Assess the morphology of the red blood cells.
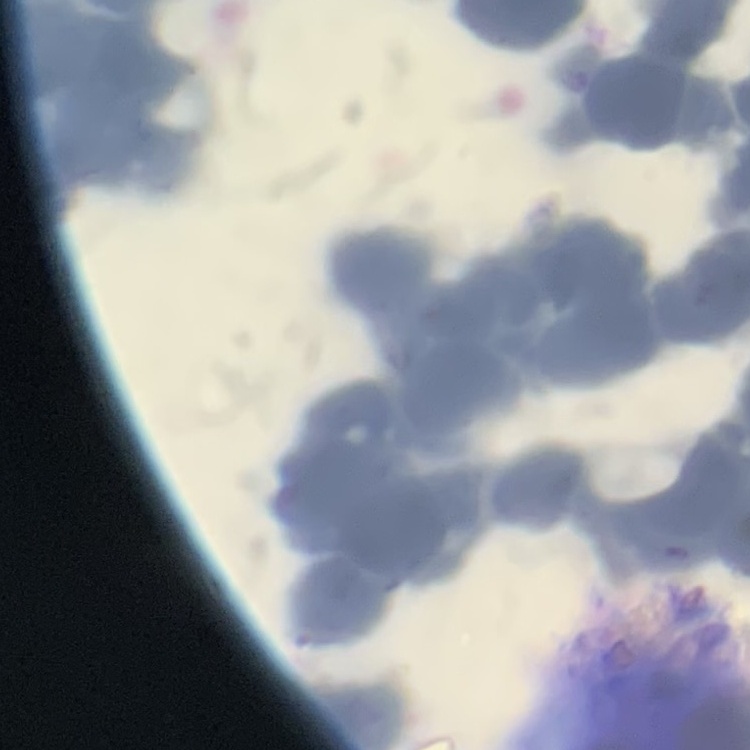
Rouleaux formation.

image type = square crop of a larger photomicrograph
preparation = thin blood smear
stain = Field's or Giemsa